Give the position of every malaria parasite.
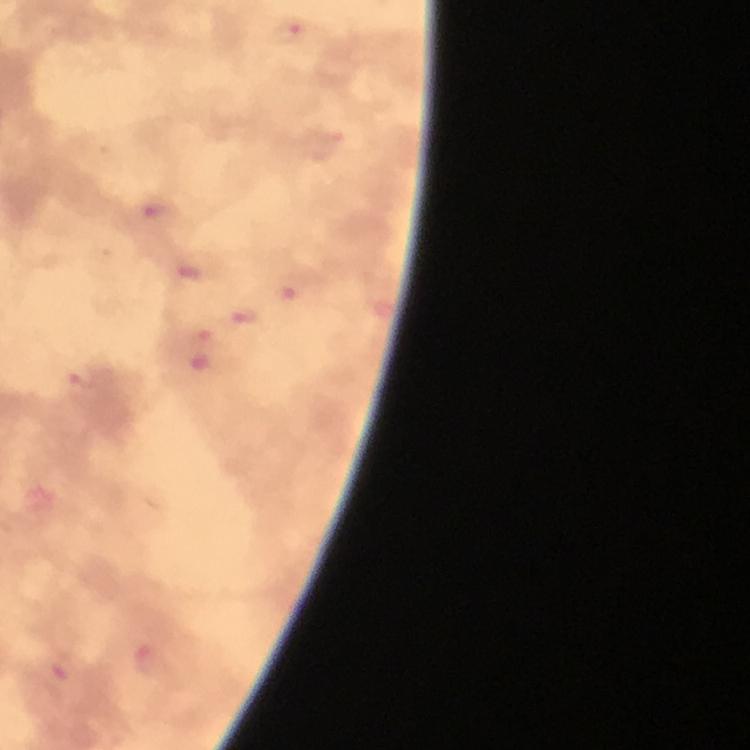
Approximate centers as {x, y} in pixels.
Malaria parasites: {289, 32}, {153, 211}, {190, 275}, {245, 316}, {205, 331}, {82, 377}, {146, 658}, {57, 681}.

Summary:
  - Context: from a diagnostic examination for malaria
  - Image size: 750×750 pixels
  - Immersion oil: used
  - Capture: smartphone mounted on the microscope
  - Stain: Giemsa
  - Magnification: 100x
  - Cropped from: one field of view
  - Preparation: thick smear